Assess this cell for malaria.
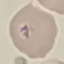

Uninfected.

Summary:
  - Image type: cell patch, automatically extracted from a larger field of view and resized to 64 × 64 pixels
  - Preparation: thin smear
  - Capture: smartphone through the microscope eyepiece
  - Stain: Giemsa